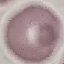
Malaria status: uninfected. Acquired by smartphone through the microscope eyepiece. Giemsa-stained preparation. Thin smear of blood. Cell patch, automatically extracted from a larger field of view and resized to 64 × 64 pixels.